Classify this cell by malaria status.
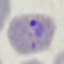
Parasitized.

Giemsa stain. Automatically extracted cell patch, resized to 64 × 64 pixels. Thin blood film. Photographed with a smartphone camera at the microscope eyepiece.